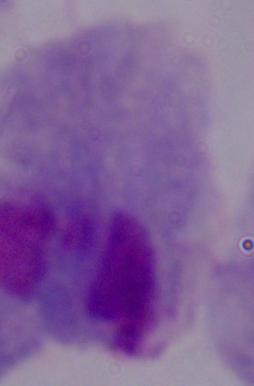

A trichomonad is shown. Micrograph. Captured at 1000x magnification.